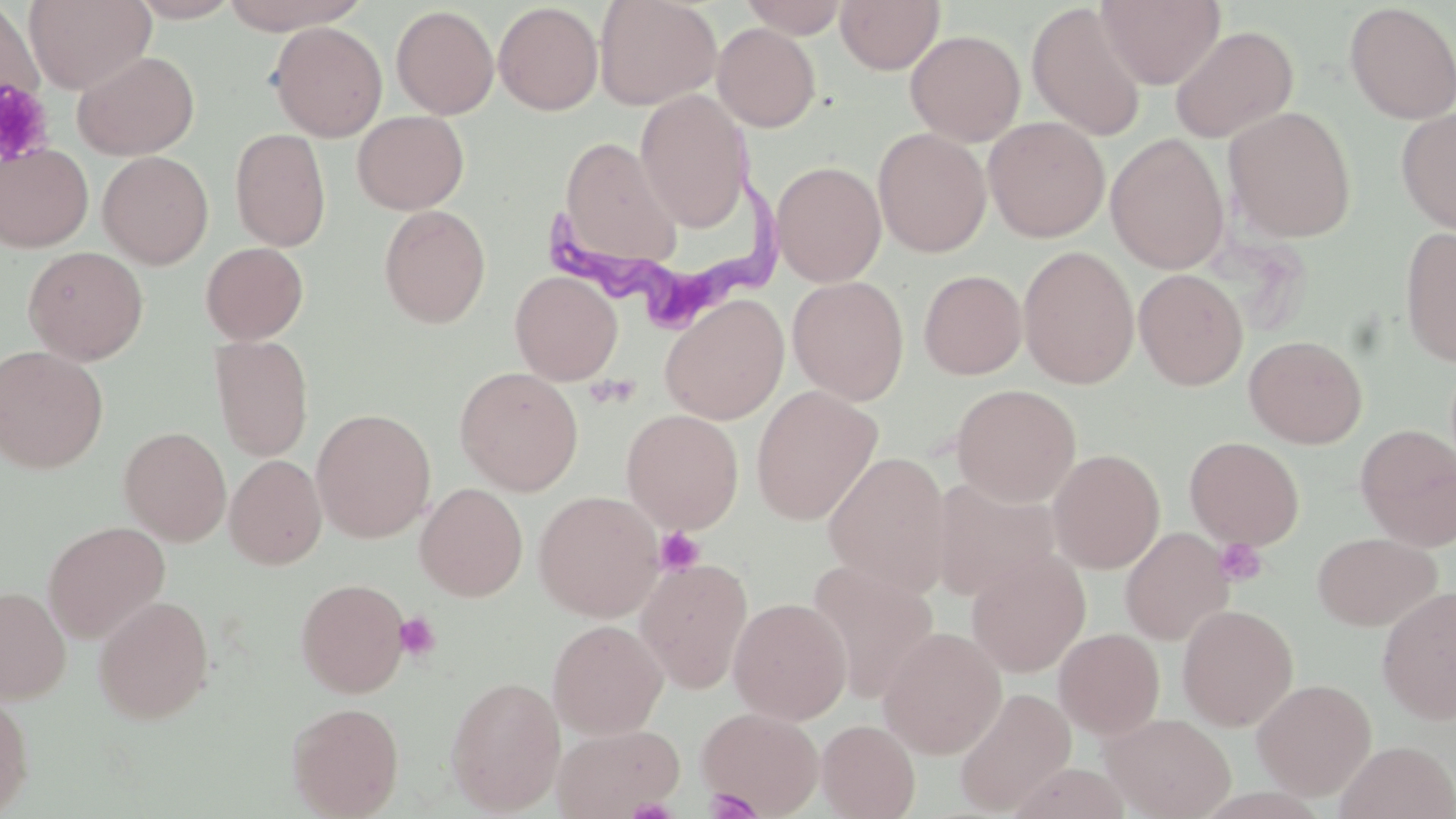
slide-level diagnosis = Trypanosoma brucei
image size = 1456×819 pixels
Trypanosoma brucei locations = approximate bounding boxes as [x1, y1, x2, y2] in pixels: [531, 160, 791, 325]
uninfected red blood cell locations = approximate bounding boxes as [x1, y1, x2, y2] in pixels: [24, 0, 155, 94], [127, 0, 242, 23], [217, 0, 370, 34], [595, 0, 722, 109], [738, 0, 851, 38], [835, 0, 945, 74], [1096, 0, 1225, 89], [0, 2, 44, 124], [493, 2, 604, 115], [1344, 2, 1456, 124], [1025, 3, 1148, 142], [391, 5, 499, 119], [268, 22, 388, 142], [712, 22, 821, 132], [1170, 25, 1299, 143], [905, 29, 1026, 146], [72, 49, 200, 160], [635, 89, 753, 232], [1224, 106, 1357, 243], [1396, 107, 1456, 235], [352, 110, 469, 214], [984, 117, 1110, 242], [873, 127, 992, 258], [230, 128, 331, 251], [1105, 133, 1230, 274], [558, 136, 681, 268], [0, 143, 94, 252], [97, 151, 213, 269], [771, 160, 887, 286], [378, 205, 491, 328], [1399, 227, 1456, 368], [200, 242, 309, 345], [1018, 245, 1140, 389], [23, 246, 149, 365], [1134, 268, 1248, 391], [918, 269, 1027, 379], [510, 271, 623, 385], [787, 276, 909, 404], [660, 294, 789, 425], [209, 334, 314, 462], [1244, 335, 1367, 448], [0, 345, 108, 473], [454, 367, 584, 495], [951, 384, 1081, 506], [750, 385, 883, 525], [311, 408, 436, 542], [621, 409, 744, 533], [1355, 424, 1456, 552], [118, 426, 231, 545], [1184, 436, 1305, 550], [1047, 448, 1165, 573], [822, 450, 952, 597], [225, 454, 327, 570], [930, 477, 1061, 602], [414, 482, 528, 601], [533, 490, 664, 621], [43, 520, 170, 644], [1120, 527, 1233, 645], [1312, 532, 1442, 631], [966, 550, 1091, 677], [635, 557, 753, 692], [808, 562, 939, 703], [296, 578, 410, 697], [1, 586, 71, 703], [1377, 586, 1456, 724], [93, 594, 214, 724], [728, 597, 852, 725], [1177, 604, 1298, 731], [547, 619, 668, 738], [878, 627, 1006, 759], [1053, 628, 1165, 739], [444, 675, 566, 814], [1252, 678, 1377, 799], [953, 686, 1076, 816], [0, 691, 33, 817], [286, 701, 404, 818], [697, 706, 824, 816], [1101, 713, 1235, 819], [816, 719, 920, 818], [552, 722, 685, 818], [1335, 740, 1456, 819], [1005, 762, 1132, 819]
stain = May-Grünwald-Giemsa
platelet locations = approximate bounding boxes as [x1, y1, x2, y2] in pixels: [0, 81, 54, 168], [654, 527, 706, 575], [1213, 538, 1268, 587], [394, 611, 441, 661], [703, 788, 762, 818]
field of view = single
modality = optical microscopy
magnification = 1000x
preparation = thin blood film